Give the position of every malaria parasite.
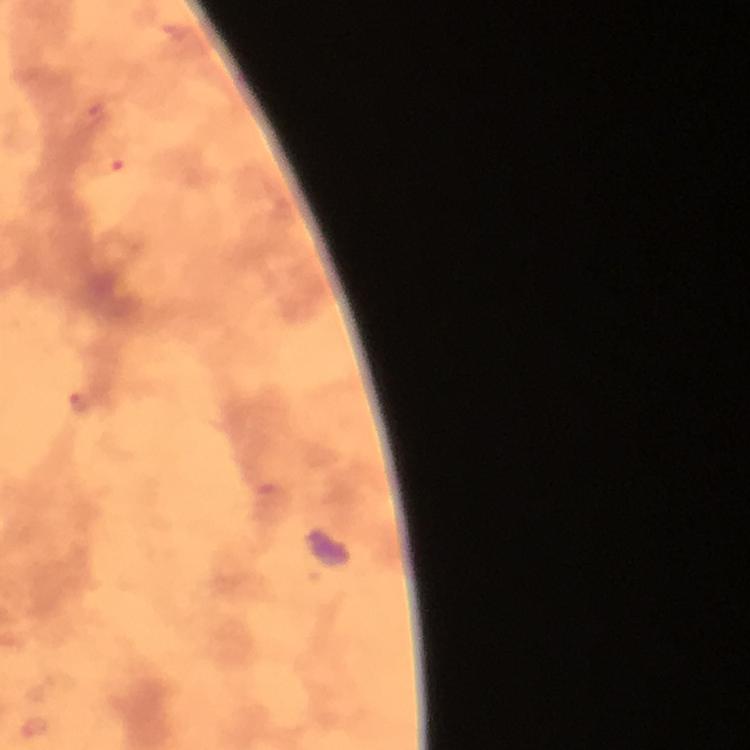
Approximate object centers, in pixels from the top-left corner.
Malaria parasites: (x=94, y=110), (x=108, y=165), (x=79, y=401), (x=36, y=728).

From a diagnostic examination for malaria. Image is 750×750 pixels. Immersion oil was used. 100x magnification. A crop from one field of view. Thick blood smear. Photographed through the microscope with a smartphone camera. Giemsa stain.